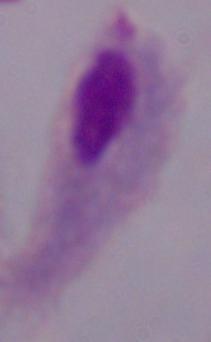 A trichomonad is seen. 1000x magnification. Photomicrograph.